Locate every Plasmodium ovale-infected red blood cell.
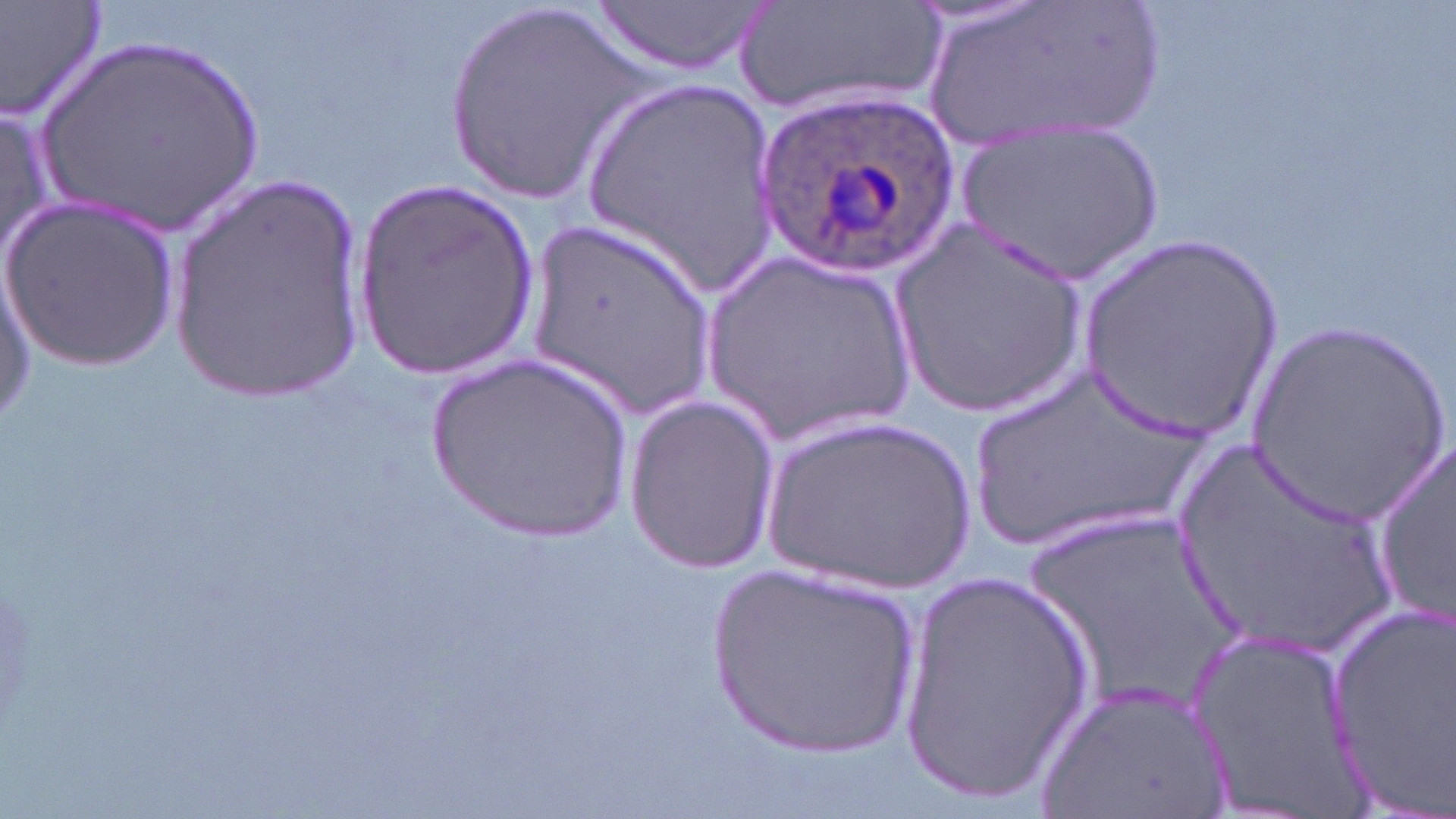

Approximate bounding boxes as named x1/y1/x2/y2 corners in pixels.
Plasmodium ovale-infected red blood cells: (x1=756, y1=92, x2=958, y2=274).

slide-level diagnosis = Plasmodium ovale
image size = 1456×819 pixels
preparation = thin blood smear
uninfected red blood cell locations = approximate bounding boxes as named x1/y1/x2/y2 corners in pixels: (x1=0, y1=0, x2=109, y2=124), (x1=729, y1=0, x2=943, y2=119), (x1=922, y1=0, x2=1162, y2=146), (x1=596, y1=1, x2=765, y2=76), (x1=439, y1=5, x2=639, y2=204), (x1=35, y1=31, x2=273, y2=240), (x1=583, y1=78, x2=782, y2=285), (x1=0, y1=102, x2=60, y2=262), (x1=956, y1=118, x2=1167, y2=284), (x1=167, y1=175, x2=371, y2=400), (x1=355, y1=178, x2=541, y2=383), (x1=1, y1=197, x2=180, y2=371), (x1=891, y1=215, x2=1089, y2=419), (x1=531, y1=218, x2=717, y2=419), (x1=1076, y1=235, x2=1284, y2=443), (x1=0, y1=248, x2=37, y2=433), (x1=702, y1=249, x2=921, y2=448), (x1=1239, y1=318, x2=1454, y2=520), (x1=426, y1=354, x2=632, y2=541), (x1=959, y1=363, x2=1219, y2=562), (x1=621, y1=394, x2=778, y2=576), (x1=763, y1=414, x2=980, y2=597), (x1=1372, y1=430, x2=1454, y2=632), (x1=1168, y1=435, x2=1400, y2=664), (x1=1023, y1=507, x2=1254, y2=720), (x1=704, y1=557, x2=924, y2=763), (x1=896, y1=567, x2=1100, y2=803), (x1=1324, y1=595, x2=1455, y2=802), (x1=1181, y1=615, x2=1367, y2=819), (x1=1037, y1=677, x2=1233, y2=817)
modality = optical microscopy
stain = May-Grünwald-Giemsa
magnification = 1000x
field of view = one of a larger specimen